State the blood parasite species.
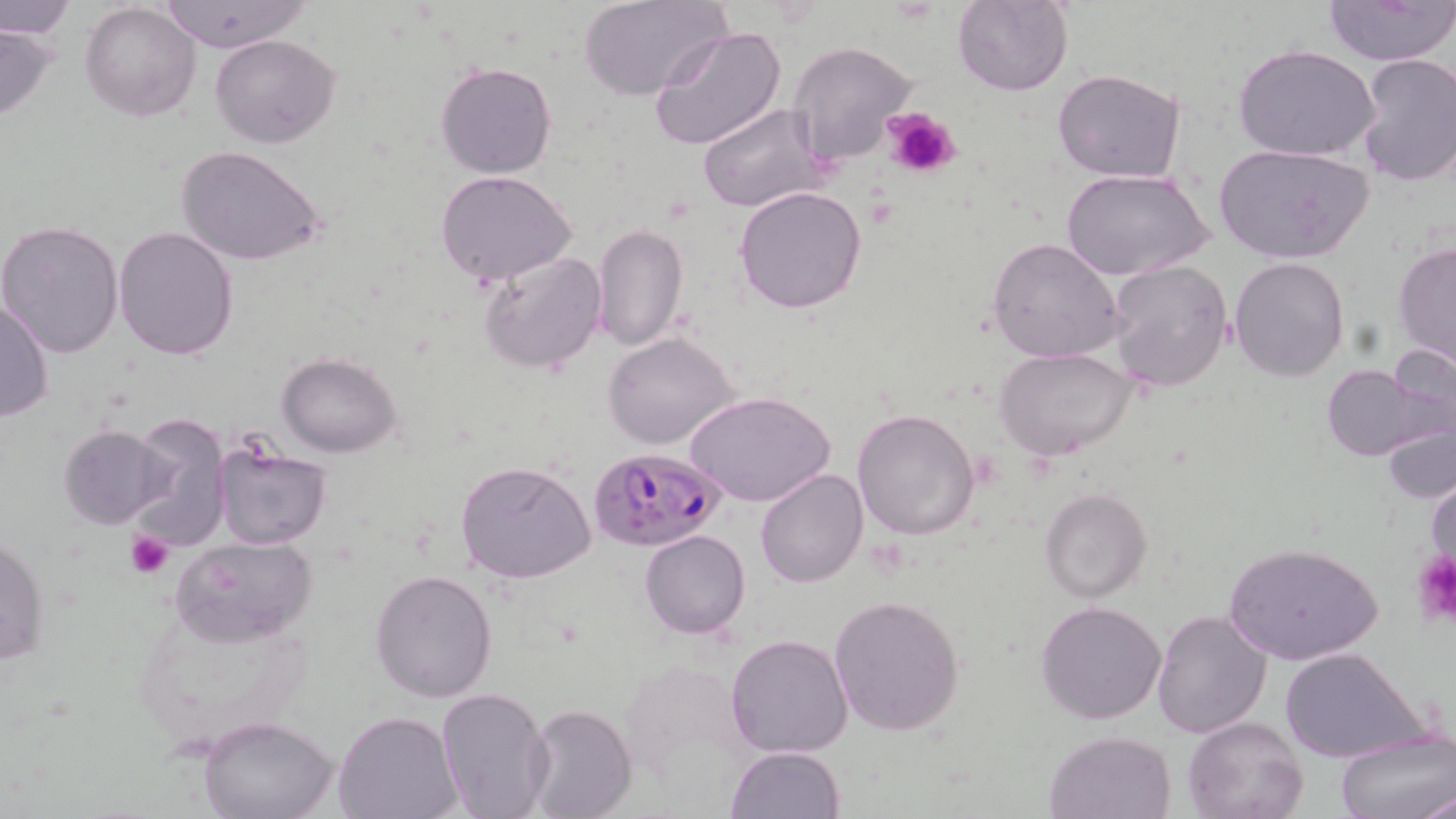

Plasmodium falciparum.

Summary:
  - Coordinate format: approximate bounding boxes as named x1/y1/x2/y2 corners in pixels
  - Uninfected red blood cell locations: (x1=0, y1=0, x2=75, y2=40), (x1=158, y1=0, x2=314, y2=53), (x1=579, y1=0, x2=731, y2=101), (x1=1322, y1=0, x2=1456, y2=66), (x1=80, y1=1, x2=201, y2=120), (x1=952, y1=1, x2=1074, y2=97), (x1=0, y1=21, x2=55, y2=123), (x1=648, y1=24, x2=788, y2=152), (x1=212, y1=33, x2=340, y2=148), (x1=787, y1=41, x2=918, y2=165), (x1=1234, y1=44, x2=1379, y2=162), (x1=1357, y1=53, x2=1456, y2=188), (x1=436, y1=62, x2=557, y2=180), (x1=1052, y1=68, x2=1187, y2=183), (x1=698, y1=100, x2=832, y2=213), (x1=1213, y1=143, x2=1374, y2=265), (x1=177, y1=144, x2=327, y2=266), (x1=1062, y1=166, x2=1213, y2=280), (x1=435, y1=169, x2=577, y2=285), (x1=735, y1=186, x2=868, y2=315), (x1=1, y1=220, x2=124, y2=358), (x1=592, y1=224, x2=688, y2=352), (x1=114, y1=225, x2=238, y2=361), (x1=986, y1=237, x2=1126, y2=363), (x1=1393, y1=241, x2=1456, y2=370), (x1=478, y1=250, x2=605, y2=375), (x1=1229, y1=256, x2=1350, y2=381), (x1=1105, y1=260, x2=1234, y2=394), (x1=0, y1=296, x2=53, y2=423), (x1=603, y1=332, x2=740, y2=450), (x1=995, y1=347, x2=1139, y2=462), (x1=277, y1=353, x2=402, y2=457), (x1=1322, y1=363, x2=1439, y2=463), (x1=683, y1=390, x2=835, y2=508), (x1=852, y1=408, x2=982, y2=541), (x1=1379, y1=411, x2=1456, y2=505), (x1=129, y1=420, x2=230, y2=553), (x1=59, y1=425, x2=174, y2=529), (x1=212, y1=441, x2=333, y2=550), (x1=455, y1=459, x2=595, y2=583), (x1=1427, y1=466, x2=1455, y2=592), (x1=754, y1=468, x2=867, y2=587), (x1=1041, y1=489, x2=1152, y2=602), (x1=641, y1=530, x2=750, y2=639), (x1=0, y1=532, x2=50, y2=668), (x1=172, y1=536, x2=318, y2=646), (x1=1223, y1=540, x2=1384, y2=666), (x1=369, y1=568, x2=497, y2=703), (x1=828, y1=595, x2=964, y2=737), (x1=1036, y1=599, x2=1167, y2=724), (x1=136, y1=602, x2=311, y2=749), (x1=1150, y1=609, x2=1272, y2=738), (x1=725, y1=633, x2=854, y2=758), (x1=1280, y1=647, x2=1429, y2=764), (x1=435, y1=687, x2=554, y2=819), (x1=522, y1=704, x2=637, y2=819), (x1=334, y1=712, x2=459, y2=819), (x1=1182, y1=714, x2=1308, y2=819), (x1=199, y1=715, x2=338, y2=819), (x1=1045, y1=730, x2=1176, y2=817), (x1=1335, y1=730, x2=1456, y2=819), (x1=725, y1=746, x2=844, y2=819), (x1=1417, y1=787, x2=1455, y2=819)
  - Plasmodium falciparum-infected red blood cell locations: (x1=590, y1=447, x2=727, y2=552)
  - Platelet locations: (x1=883, y1=109, x2=960, y2=178), (x1=127, y1=532, x2=173, y2=578), (x1=1411, y1=550, x2=1456, y2=626)
  - Stain: May-Grünwald-Giemsa
  - Field of view: one of a larger specimen
  - Magnification: 1000x
  - Modality: light microscopy
  - Image size: 1456×819 pixels
  - Preparation: thin blood film